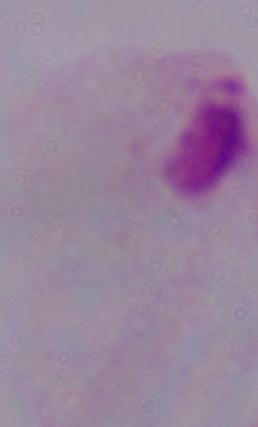
A trichomonad is shown. 1000x magnification. Photomicrograph.